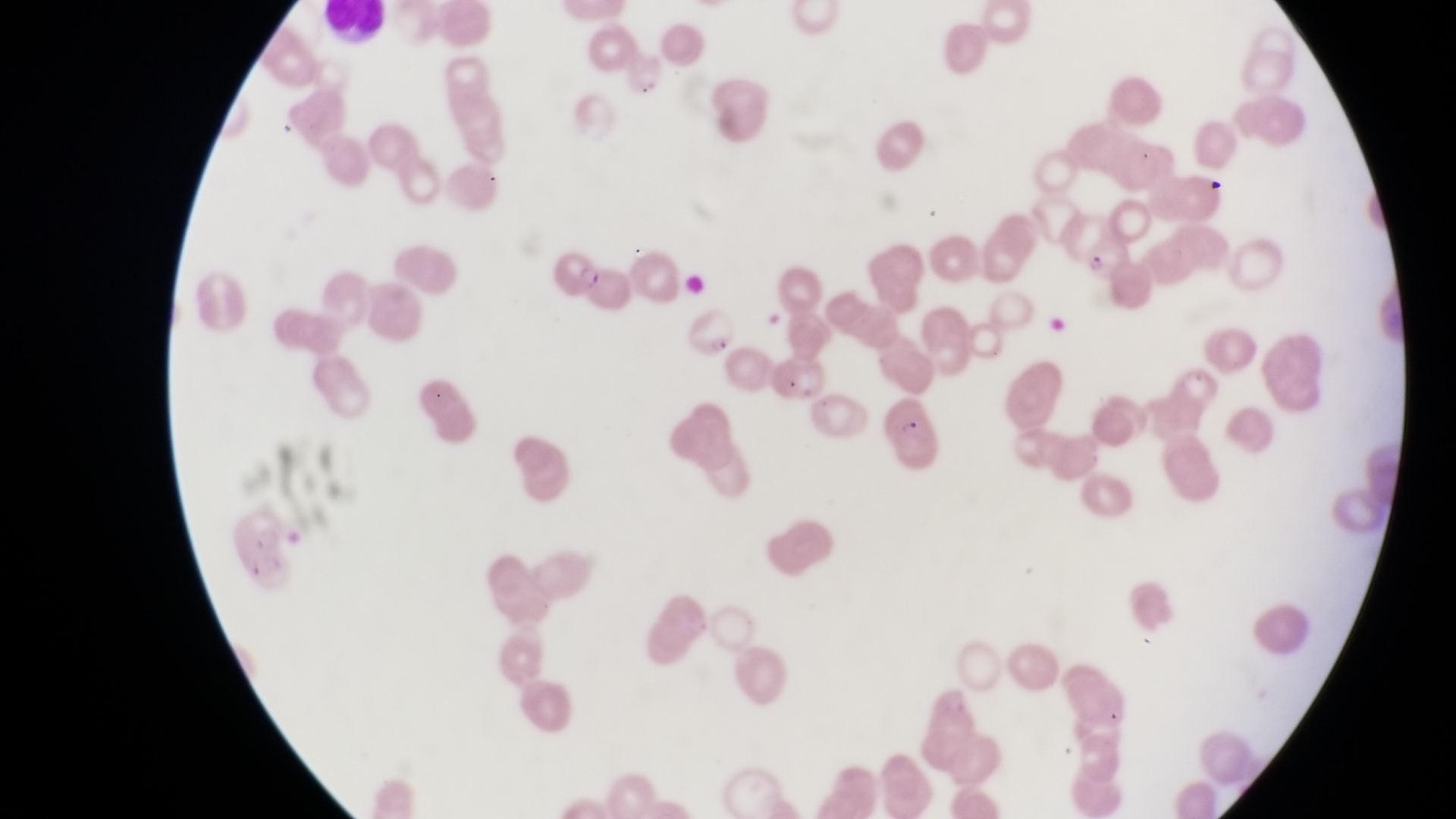 Approximate bounding boxes as left top right bottom in pixels. Parasitised red blood cell locations: 1081 237 1134 286; 549 246 605 295; 689 304 741 356; 880 396 943 469. Leukocyte locations: 322 4 390 44. Sample from Uganda. Single field of view. Magnification of 1000x. Photographed through the eyepiece of an Olympus CX-23 microscope with a smartphone camera. Image is 1456×819 pixels. Thin blood film.